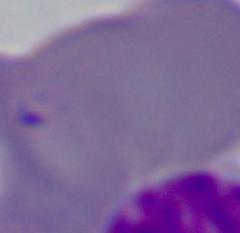

modality: photomicrograph
magnification: 1000x
identification: Babesia